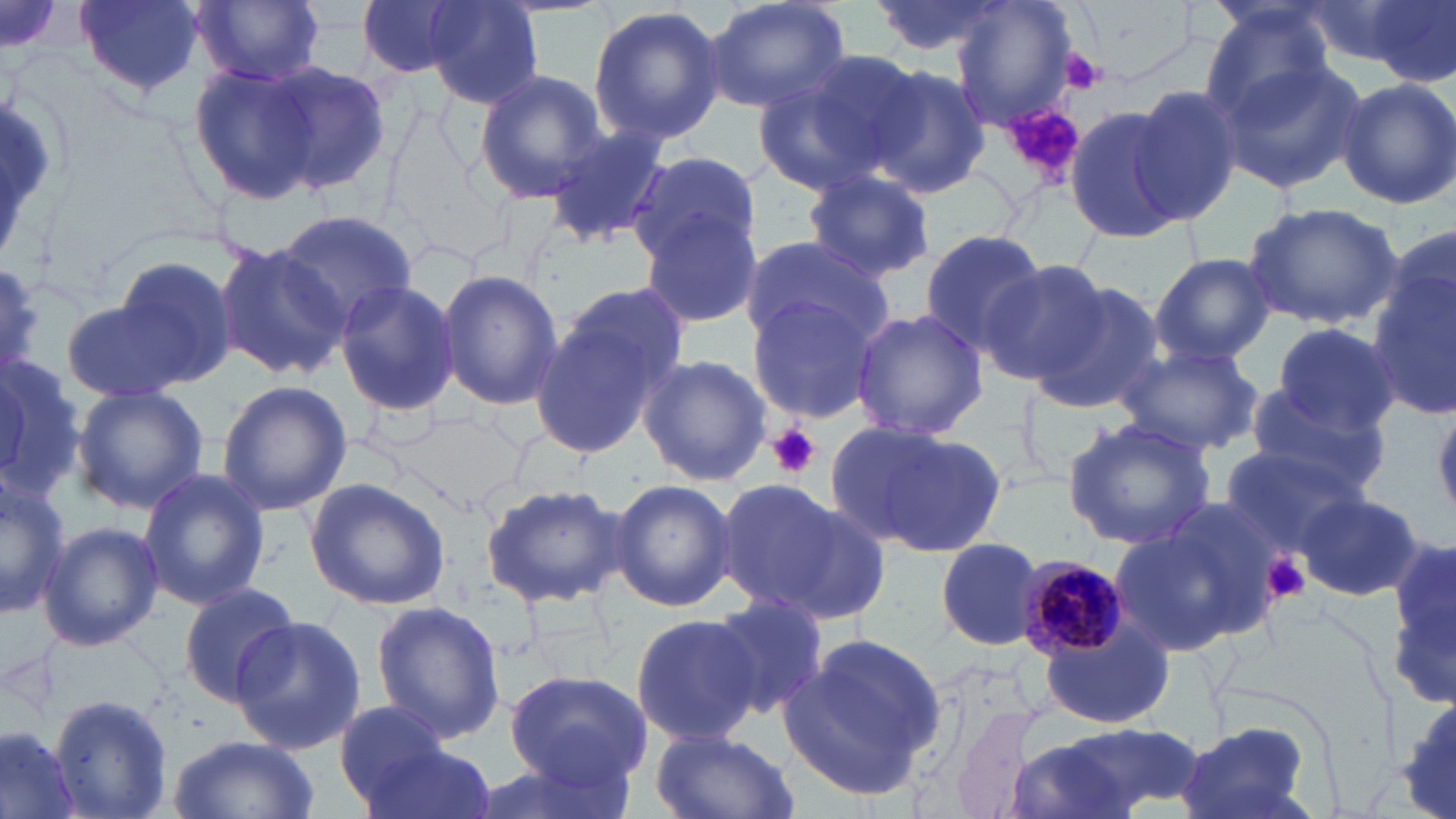
Approximate bounding boxes as [x1, y1, x2, y2] in pixels. Plasmodium malariae-infected red blood cell locations: [1016, 554, 1130, 658]. Uninfected red blood cell locations: [77, 0, 205, 96], [194, 0, 326, 86], [357, 0, 473, 79], [702, 0, 852, 114], [865, 0, 1015, 59], [948, 0, 1080, 131], [1357, 0, 1456, 86], [422, 1, 543, 108], [586, 3, 726, 145], [1197, 3, 1338, 121], [1212, 53, 1368, 195], [751, 54, 921, 195], [187, 61, 322, 206], [263, 61, 391, 194], [864, 63, 992, 200], [472, 70, 609, 204], [1336, 76, 1456, 211], [1126, 85, 1244, 224], [1064, 105, 1183, 244], [542, 125, 670, 247], [626, 150, 762, 271], [799, 170, 938, 283], [1241, 200, 1404, 328], [273, 210, 417, 328], [639, 212, 763, 327], [918, 229, 1050, 356], [739, 233, 892, 352], [214, 241, 347, 384], [1150, 253, 1276, 365], [112, 255, 236, 387], [975, 261, 1115, 384], [1368, 261, 1454, 417], [437, 268, 562, 411], [333, 277, 460, 418], [1029, 281, 1168, 417], [532, 288, 685, 457], [744, 289, 887, 427], [62, 299, 191, 402], [850, 308, 987, 442], [1273, 321, 1399, 435], [0, 344, 84, 514], [1113, 344, 1264, 455], [638, 353, 771, 487], [217, 380, 352, 516], [1245, 383, 1392, 503], [70, 387, 208, 515], [386, 407, 531, 513], [1061, 416, 1217, 550], [834, 420, 1008, 558], [1220, 444, 1365, 559], [138, 466, 270, 611], [0, 476, 68, 617], [304, 478, 450, 611], [609, 478, 738, 613], [715, 478, 850, 613], [480, 483, 630, 609], [775, 491, 894, 627], [1293, 492, 1423, 601], [1106, 513, 1266, 657], [38, 520, 163, 651], [1392, 533, 1456, 708], [934, 535, 1049, 650], [176, 581, 301, 707], [711, 594, 831, 720], [369, 600, 507, 743], [630, 611, 764, 748], [230, 615, 366, 755], [1039, 623, 1177, 726], [779, 635, 948, 801], [500, 667, 654, 797], [49, 694, 175, 819], [332, 701, 458, 815], [951, 709, 1062, 819], [1052, 722, 1207, 811], [1173, 723, 1316, 819], [1, 726, 84, 819], [647, 726, 798, 819], [167, 734, 320, 819], [355, 735, 498, 819], [1000, 737, 1149, 819], [466, 754, 638, 819]. Platelet locations: [1058, 49, 1105, 94], [1003, 106, 1086, 187], [764, 423, 821, 479], [1262, 551, 1310, 602]. Slide-level diagnosis: Plasmodium malariae. Image is 1456×819 pixels. One field of a larger specimen. Optical microscopy. Thin blood smear. 1000x magnification. May-Grünwald-Giemsa-stained preparation.